Comment on the morphology of the red blood cells.
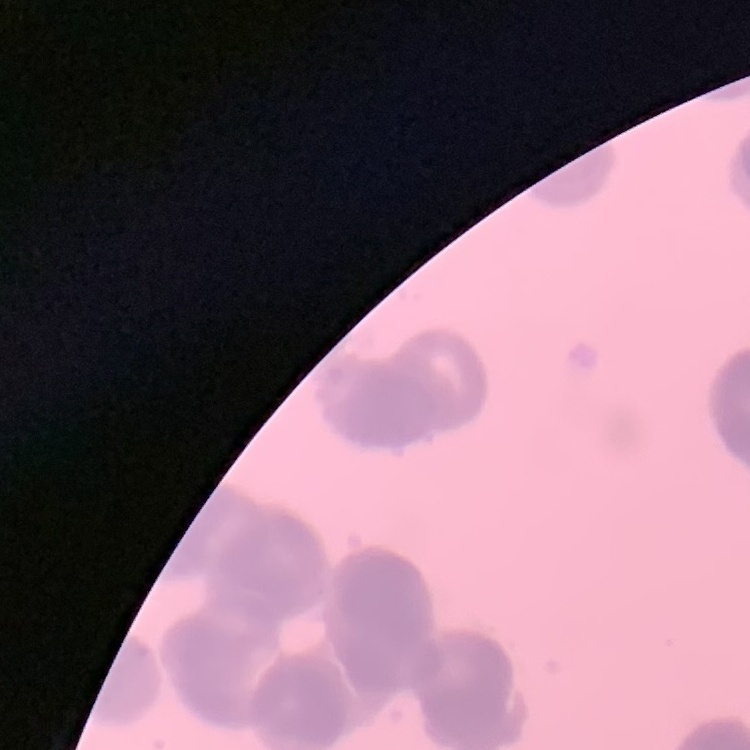
Rouleaux formation.

Field's or Giemsa stain. Thin blood smear. One tile cut from a larger photomicrograph.